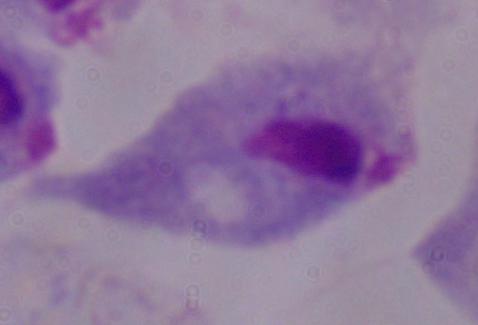
{
  "modality": "micrograph",
  "magnification": "1000x",
  "identification": "trichomonad"
}